Report the malaria status of this cell.
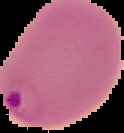

Parasitized.

Summary:
  - Image size: 124×133 pixels
  - Image type: segmented cell region with the area outside set to black
  - Preparation: thin blood film